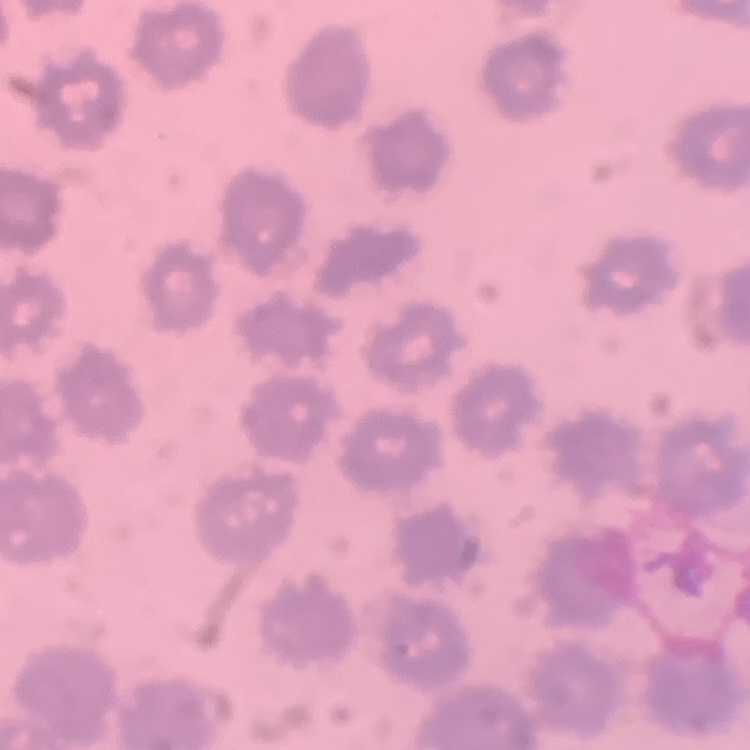
erythrocyte morphology = no rouleaux formation
preparation = thin peripheral smear
image type = square crop of a larger photomicrograph
stain = Field's or Giemsa